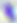
Summary:
  - Modality: photomicrograph
  - Identification: Toxoplasma gondii
  - Magnification: 400x